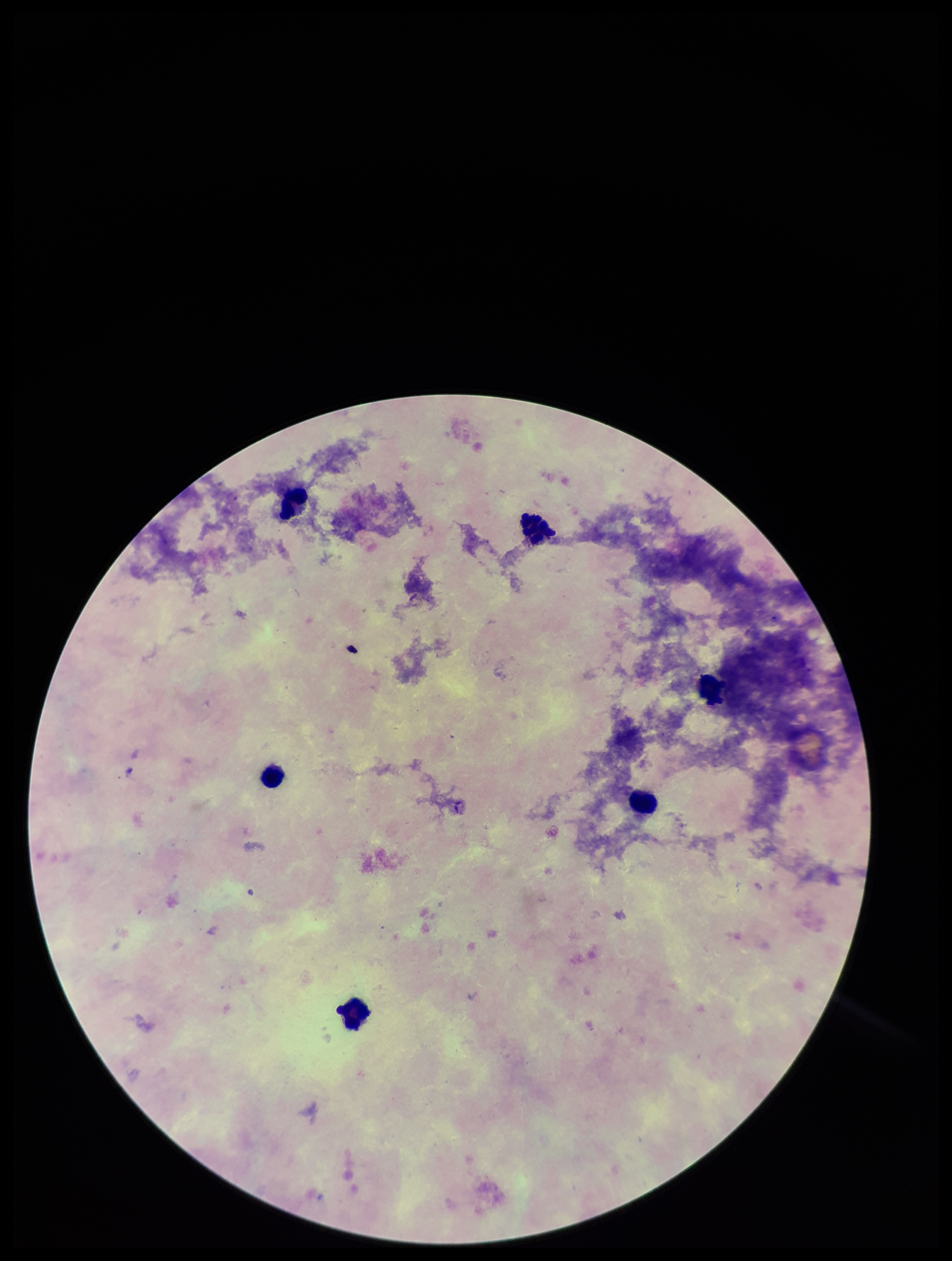
field of view = one from this slide
leukocyte count = 6
capture = smartphone photograph through the microscope eyepiece
preparation = thick
image size = 952×1261 pixels
stain = Giemsa
Plasmodium parasites = none seen
parasite count = 0
patient malaria status = negative